Locate every leukocyte (white blood cell).
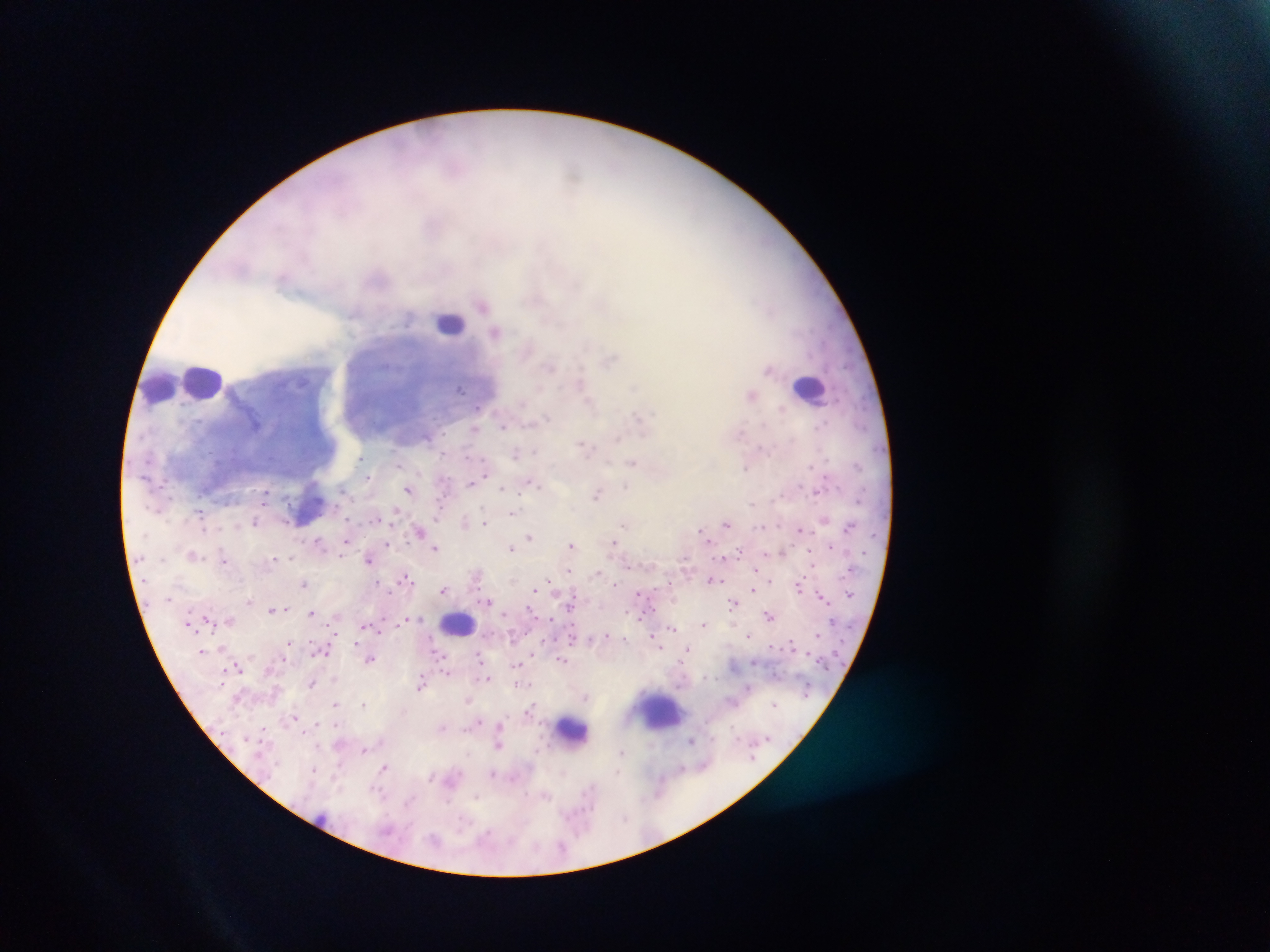

Approximate centers as x y in pixels.
Leukocytes: 449 322; 205 382; 159 386; 810 388; 308 508; 458 622; 663 710; 573 730.

field_of_view: single
image_size: 1270×952 pixels
country: Ghana
preparation: thick blood smear
plasmodium_parasite_locations: 'approximate centers as x y in pixels: 482 305; 496 331; 549 366; 460 389; 478 407; 781 409; 547 416; 638 416; 820 425; 503 426; 475 429; 427 436; 583 444; 761 448; 535 450; 516 453; 360 459; 634 463; 857 464; 398 465; 810 465; 745 467; 485 469; 367 476; 475 480; 470 483; 533 483; 626 487; 342 488; 503 488; 408 490; 266 493; 598 493; 752 503; 439 510; 200 512; 396 512; 512 513; 376 518; 347 519; 255 522; 464 522; 485 523; 623 524; 726 524; 761 526; 849 527; 203 529; 800 529; 700 530; 419 531; 530 537; 318 541; 388 543; 343 544; 615 544; 571 545; 831 546; 436 548; 510 549; 739 551; 783 552; 342 554; 193 555; 273 558; 291 558; 367 559; 223 560; 756 569; 569 571; 476 576; 406 578; 712 580; 549 581; 616 583; 303 584; 379 584; 800 587; 754 589; 445 590; 534 590; 638 594; 822 595; 249 600; 487 601; 733 602; 571 605; 271 609; 284 609; 311 613; 769 616; 206 617; 230 619; 408 619; 551 619; 703 624; 365 625; 672 628; 606 635; 748 636; 625 638; 655 641; 288 642; 659 646; 687 648; 440 655; 478 657; 371 659; 562 659; 516 665; 238 668; 447 672; 487 678; 334 679; 312 684; 421 684; 522 684; 749 688; 586 696; 468 701; 335 703; 364 704; 775 704; 530 708; 296 717; 477 722; 335 725; 500 726; 263 728; 442 728; 691 741; 498 745; 365 750; 621 752; 383 768; 681 769; 313 770; 493 773; 430 776; 377 790; 476 796; 546 796; 409 801; 462 824; 486 833; 562 846'
capture: mobile-phone photograph through a microscope